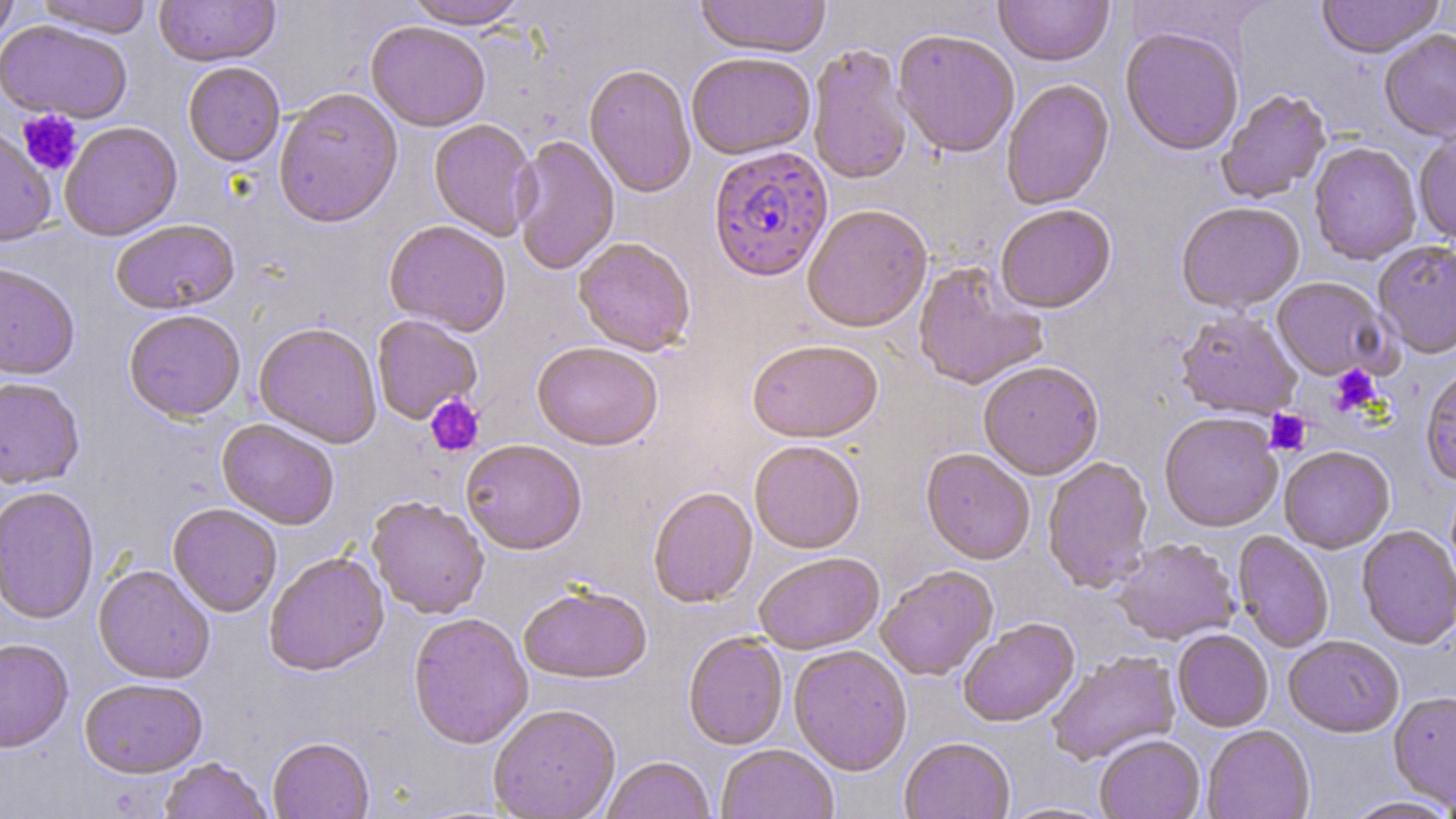
Approximate bounding boxes as named x1/y1/x2/y2 corners in pixels. Plasmodium falciparum-infected red blood cell locations: (x1=708, y1=147, x2=834, y2=283). Platelet locations: (x1=17, y1=110, x2=83, y2=176), (x1=1329, y1=365, x2=1382, y2=415), (x1=424, y1=394, x2=485, y2=457), (x1=1265, y1=410, x2=1311, y2=456). Uninfected red blood cell locations: (x1=0, y1=0, x2=19, y2=50), (x1=34, y1=0, x2=152, y2=37), (x1=154, y1=0, x2=280, y2=67), (x1=403, y1=0, x2=529, y2=29), (x1=694, y1=0, x2=830, y2=58), (x1=994, y1=0, x2=1113, y2=68), (x1=1316, y1=0, x2=1444, y2=59), (x1=0, y1=20, x2=133, y2=123), (x1=366, y1=21, x2=491, y2=132), (x1=1120, y1=27, x2=1244, y2=156), (x1=1379, y1=29, x2=1456, y2=143), (x1=893, y1=30, x2=1020, y2=159), (x1=807, y1=43, x2=913, y2=186), (x1=686, y1=52, x2=816, y2=160), (x1=183, y1=61, x2=285, y2=167), (x1=584, y1=64, x2=697, y2=199), (x1=1001, y1=79, x2=1114, y2=211), (x1=274, y1=89, x2=403, y2=229), (x1=1216, y1=89, x2=1331, y2=204), (x1=428, y1=119, x2=540, y2=242), (x1=59, y1=121, x2=182, y2=240), (x1=0, y1=124, x2=57, y2=247), (x1=1414, y1=131, x2=1456, y2=248), (x1=512, y1=135, x2=620, y2=277), (x1=1309, y1=143, x2=1421, y2=265), (x1=1176, y1=202, x2=1304, y2=314), (x1=802, y1=205, x2=932, y2=334), (x1=995, y1=205, x2=1116, y2=315), (x1=111, y1=219, x2=241, y2=314), (x1=384, y1=221, x2=511, y2=336), (x1=573, y1=238, x2=695, y2=357), (x1=1373, y1=241, x2=1456, y2=361), (x1=912, y1=261, x2=1049, y2=391), (x1=0, y1=262, x2=81, y2=379), (x1=1271, y1=278, x2=1391, y2=382), (x1=124, y1=309, x2=246, y2=422), (x1=1175, y1=310, x2=1302, y2=421), (x1=371, y1=315, x2=483, y2=425), (x1=253, y1=322, x2=382, y2=448), (x1=532, y1=342, x2=663, y2=452), (x1=748, y1=342, x2=884, y2=444), (x1=979, y1=362, x2=1104, y2=481), (x1=1420, y1=368, x2=1456, y2=487), (x1=0, y1=376, x2=85, y2=489), (x1=1159, y1=414, x2=1283, y2=533), (x1=216, y1=419, x2=340, y2=530), (x1=461, y1=440, x2=586, y2=555), (x1=749, y1=440, x2=865, y2=555), (x1=1279, y1=447, x2=1395, y2=554), (x1=920, y1=449, x2=1035, y2=565), (x1=1042, y1=456, x2=1154, y2=593), (x1=0, y1=486, x2=100, y2=625), (x1=648, y1=488, x2=757, y2=608), (x1=367, y1=497, x2=489, y2=619), (x1=168, y1=503, x2=282, y2=617), (x1=1356, y1=526, x2=1456, y2=650), (x1=1233, y1=532, x2=1334, y2=653), (x1=1112, y1=539, x2=1240, y2=647), (x1=264, y1=551, x2=389, y2=676), (x1=754, y1=554, x2=884, y2=655), (x1=93, y1=564, x2=215, y2=684), (x1=876, y1=567, x2=998, y2=681), (x1=518, y1=585, x2=652, y2=684), (x1=408, y1=613, x2=534, y2=750), (x1=958, y1=620, x2=1079, y2=728), (x1=1172, y1=630, x2=1273, y2=732), (x1=683, y1=633, x2=788, y2=750), (x1=1284, y1=636, x2=1404, y2=739), (x1=0, y1=638, x2=74, y2=754), (x1=788, y1=645, x2=912, y2=776), (x1=1047, y1=652, x2=1181, y2=766), (x1=79, y1=678, x2=208, y2=779), (x1=1388, y1=692, x2=1456, y2=811), (x1=488, y1=704, x2=621, y2=818), (x1=1202, y1=726, x2=1315, y2=819), (x1=1095, y1=736, x2=1205, y2=819), (x1=267, y1=738, x2=374, y2=819), (x1=900, y1=738, x2=1015, y2=819), (x1=716, y1=744, x2=837, y2=819), (x1=602, y1=757, x2=715, y2=819), (x1=158, y1=759, x2=271, y2=819), (x1=1343, y1=797, x2=1456, y2=819). Slide-level diagnosis: Plasmodium falciparum. May-Grünwald-Giemsa stain. Light microscopy. 1000x magnification. Image is 1456×819 pixels. Thin blood smear. One field of a larger specimen.